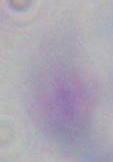

identification = Toxoplasma gondii
modality = micrograph
magnification = 1000x